Evaluate for malaria.
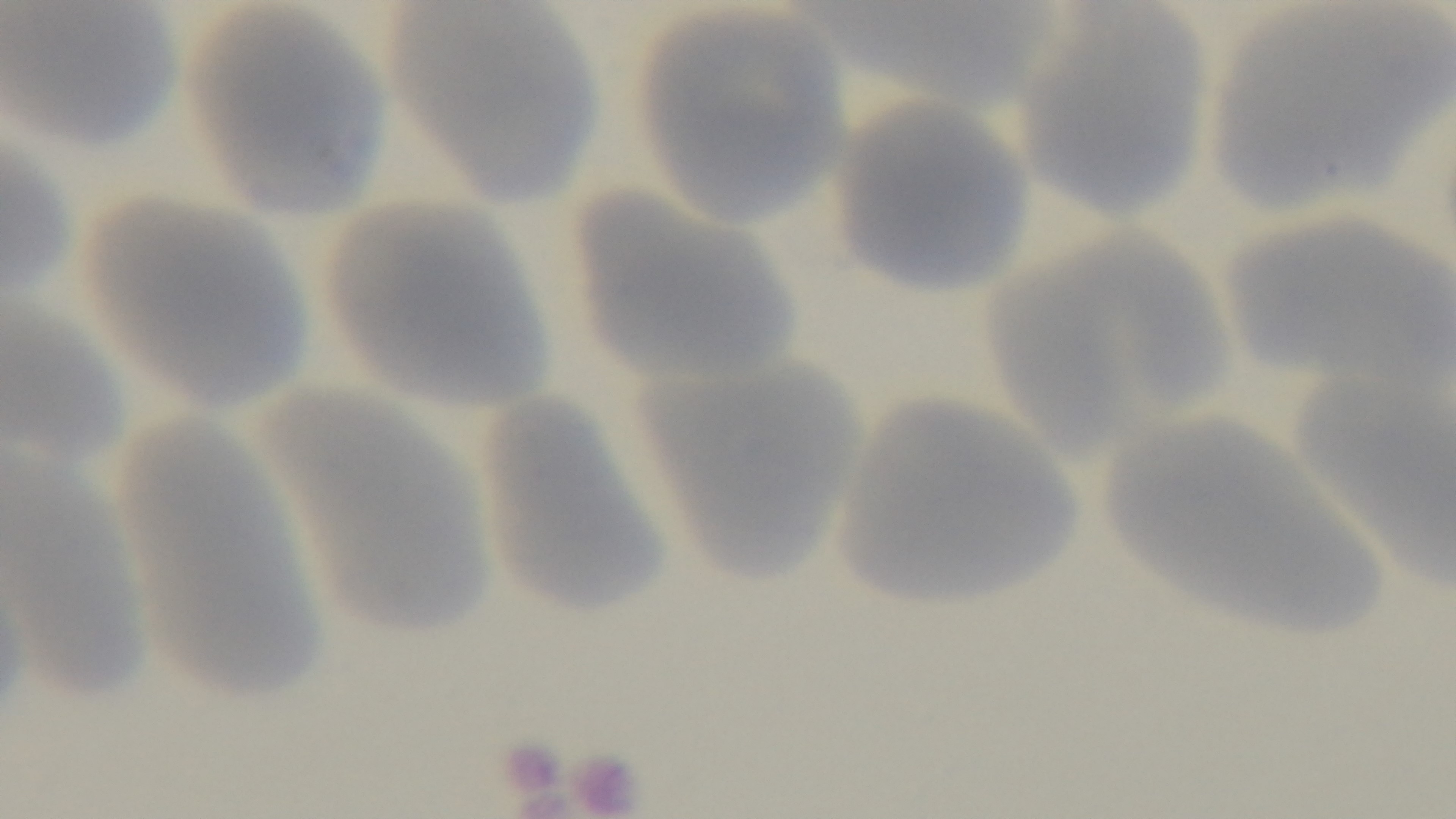
It is uninfected.

Summary:
  - Objective: 100x oil immersion
  - Field of view: single
  - Preparation: thin
  - Capture: mounted 4K digital camera
  - Stain: Giemsa
  - Modality: light microscopy